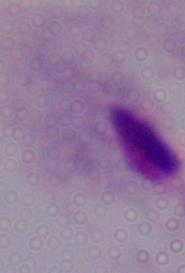
identification = trichomonad
modality = micrograph
magnification = 1000x